Classify this cell by malaria status.
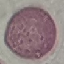
It is uninfected.

stain = Giemsa
preparation = thin blood smear
capture = smartphone through the microscope eyepiece
image type = cell patch, automatically extracted from a larger field of view and resized to 64 × 64 pixels